Locate every Plasmodium falciparum-infected red blood cell.
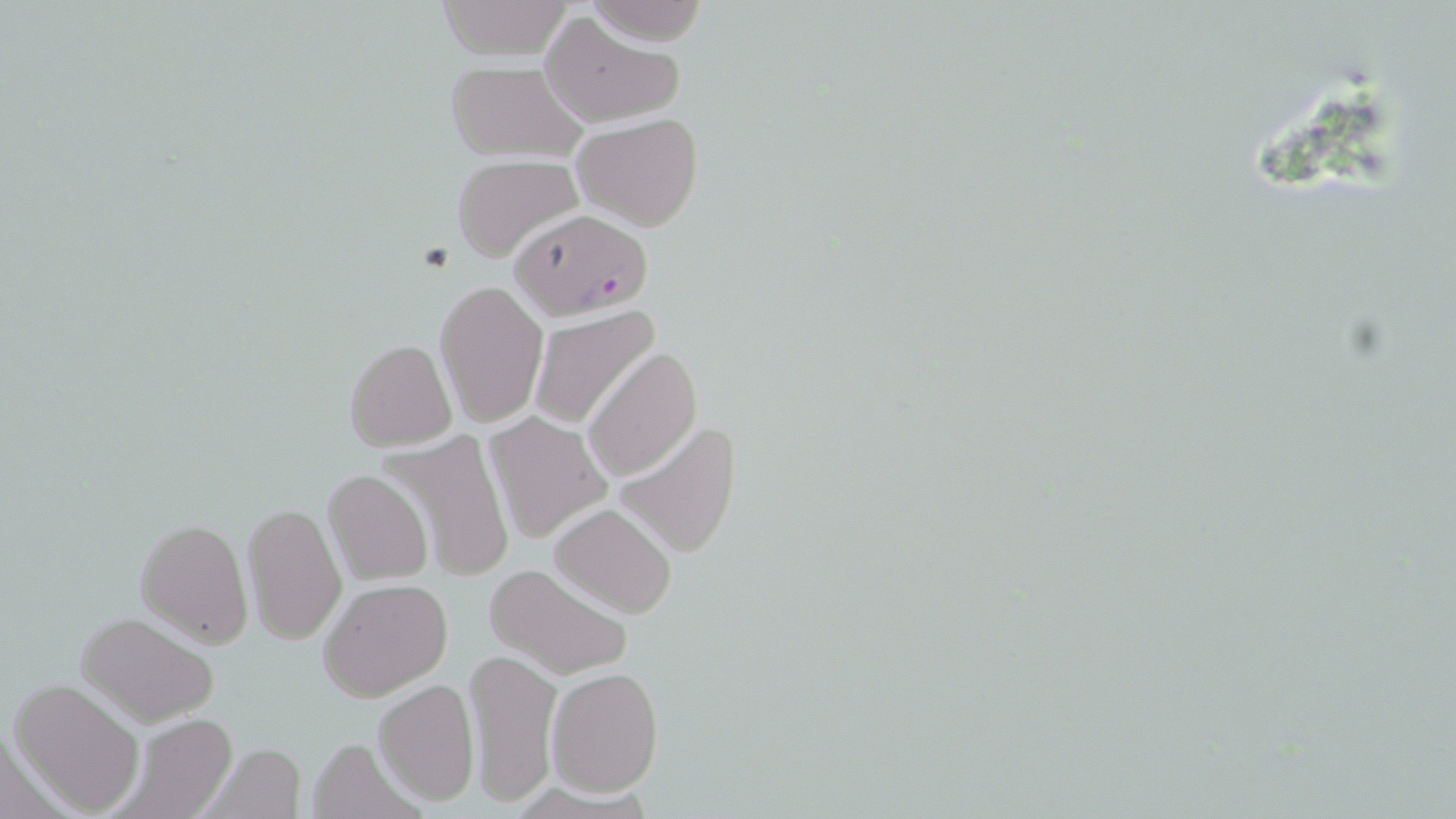

Approximate bounding boxes as named x1/y1/x2/y2 corners in pixels.
Plasmodium falciparum-infected red blood cells: (x1=508, y1=207, x2=652, y2=320).

Summary:
  - Uninfected red blood cell locations: (x1=432, y1=1, x2=574, y2=61), (x1=585, y1=2, x2=710, y2=43), (x1=540, y1=12, x2=680, y2=126), (x1=443, y1=62, x2=590, y2=164), (x1=574, y1=113, x2=705, y2=232), (x1=452, y1=154, x2=583, y2=260), (x1=435, y1=281, x2=548, y2=428), (x1=528, y1=305, x2=659, y2=430), (x1=344, y1=338, x2=456, y2=451), (x1=584, y1=347, x2=703, y2=481), (x1=484, y1=412, x2=612, y2=544), (x1=613, y1=421, x2=743, y2=560), (x1=384, y1=431, x2=515, y2=585), (x1=322, y1=468, x2=433, y2=586), (x1=272, y1=477, x2=408, y2=609), (x1=243, y1=501, x2=347, y2=645), (x1=550, y1=502, x2=677, y2=617), (x1=137, y1=517, x2=252, y2=646), (x1=486, y1=563, x2=631, y2=680), (x1=321, y1=578, x2=454, y2=701), (x1=75, y1=612, x2=222, y2=727), (x1=466, y1=647, x2=563, y2=809), (x1=548, y1=667, x2=664, y2=798), (x1=10, y1=679, x2=144, y2=815), (x1=374, y1=680, x2=479, y2=804), (x1=112, y1=711, x2=238, y2=819), (x1=304, y1=734, x2=422, y2=819), (x1=199, y1=743, x2=305, y2=818)
  - Slide-level diagnosis: Plasmodium falciparum
  - Field of view: one of a larger specimen
  - Magnification: 1000x
  - Modality: optical microscopy
  - Stain: May-Grünwald-Giemsa
  - Preparation: thin blood film
  - Image size: 1456×819 pixels